Report the malaria status.
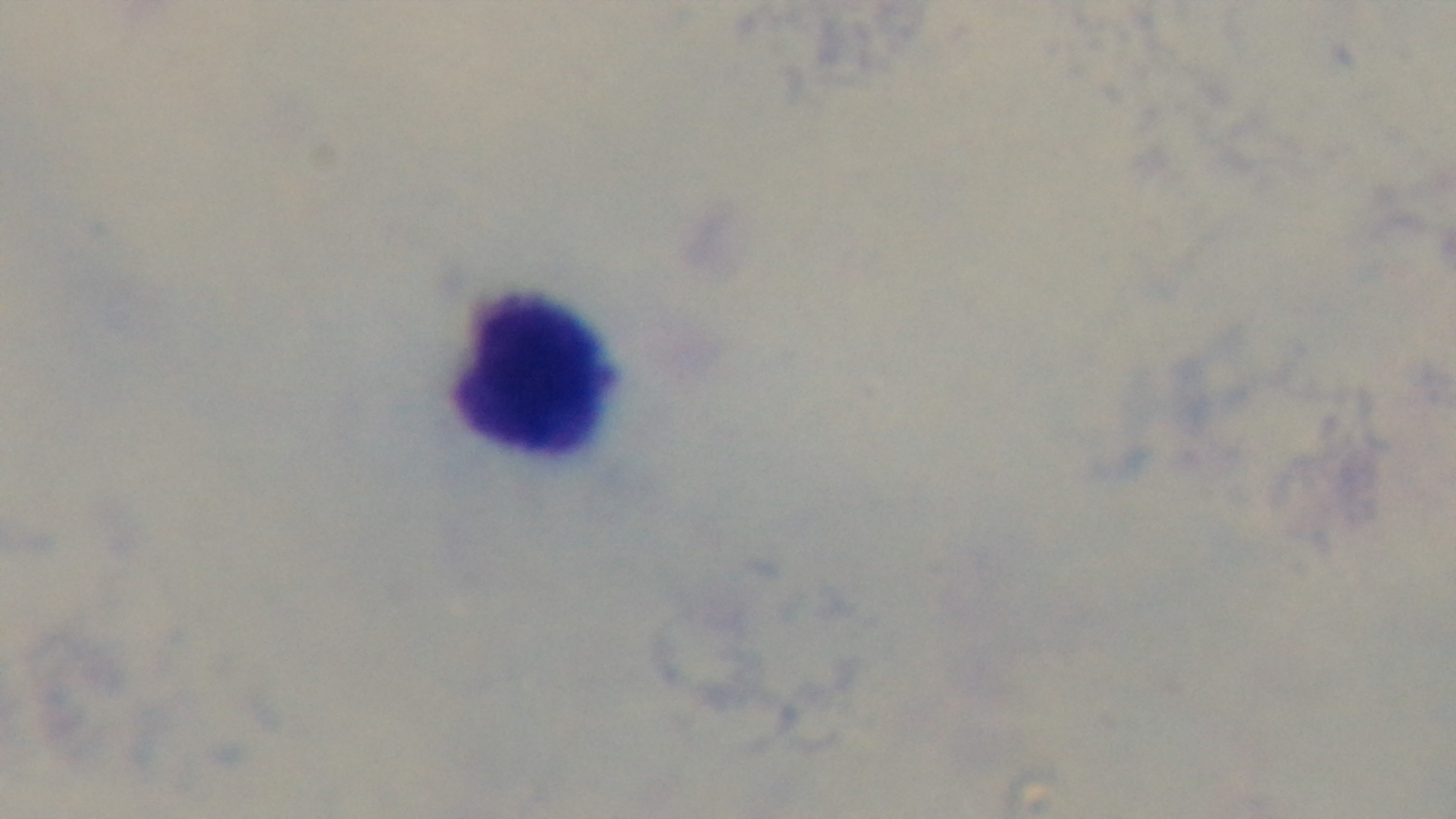

Uninfected.

Oil-immersion objective, 100x. Giemsa stain. Photomicrograph. Preparation: thick. Mounted 4K digital camera. Single field of view.